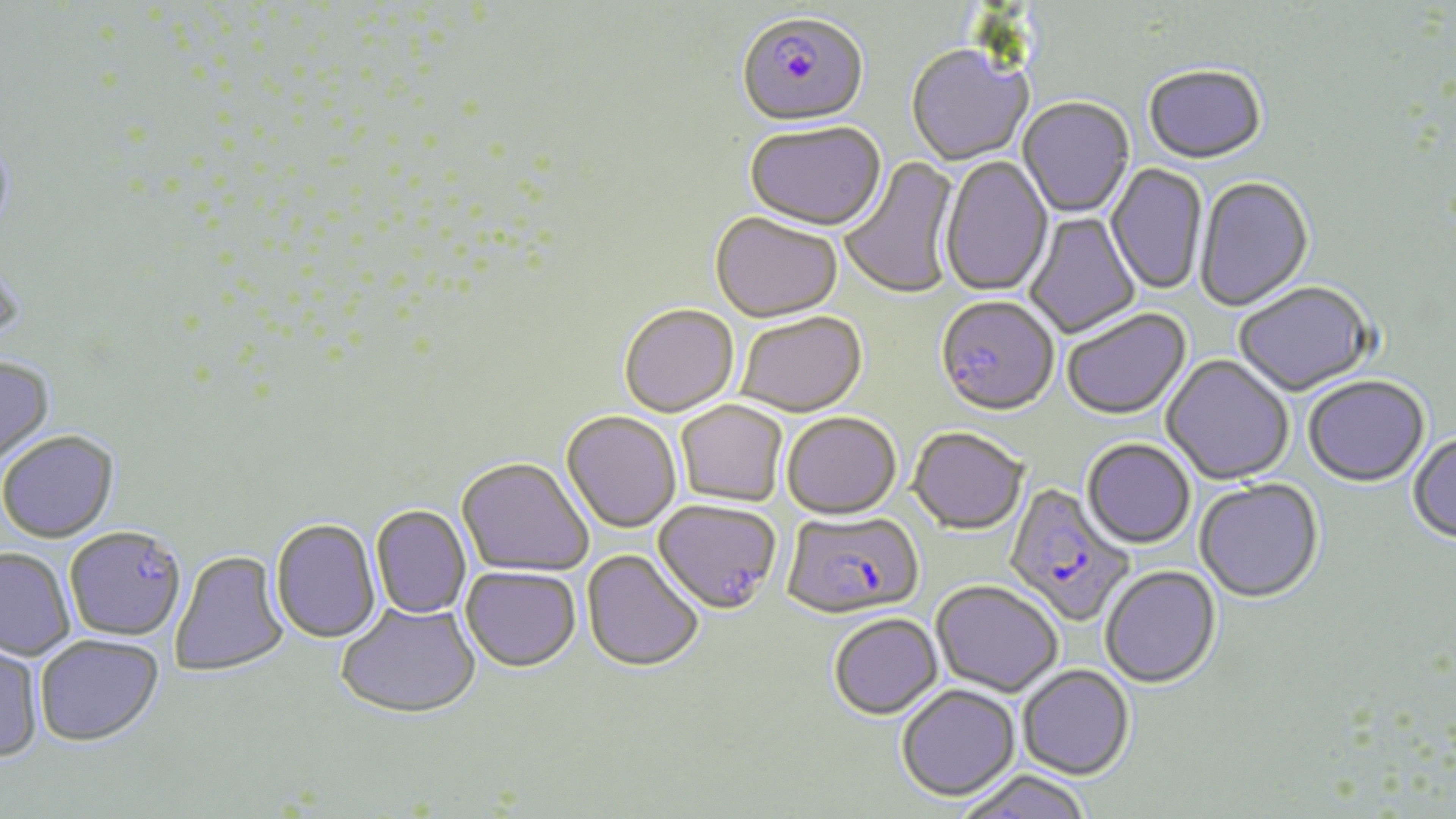

Approximate bounding boxes as named x1/y1/x2/y2 corners in pixels. Uninfected red blood cell locations: (x1=906, y1=46, x2=1033, y2=167), (x1=1143, y1=67, x2=1267, y2=167), (x1=1018, y1=98, x2=1134, y2=219), (x1=744, y1=125, x2=886, y2=234), (x1=840, y1=156, x2=962, y2=300), (x1=939, y1=156, x2=1054, y2=297), (x1=1106, y1=163, x2=1208, y2=296), (x1=1194, y1=177, x2=1315, y2=313), (x1=1024, y1=212, x2=1140, y2=339), (x1=710, y1=214, x2=844, y2=325), (x1=1233, y1=283, x2=1377, y2=398), (x1=941, y1=301, x2=1060, y2=416), (x1=619, y1=306, x2=739, y2=418), (x1=1062, y1=309, x2=1192, y2=421), (x1=737, y1=313, x2=866, y2=418), (x1=1162, y1=355, x2=1294, y2=486), (x1=0, y1=357, x2=56, y2=471), (x1=1303, y1=377, x2=1430, y2=488), (x1=676, y1=401, x2=788, y2=506), (x1=561, y1=411, x2=681, y2=533), (x1=781, y1=413, x2=902, y2=520), (x1=908, y1=426, x2=1028, y2=535), (x1=1408, y1=432, x2=1456, y2=546), (x1=0, y1=433, x2=119, y2=544), (x1=1082, y1=438, x2=1196, y2=549), (x1=456, y1=458, x2=593, y2=578), (x1=1194, y1=478, x2=1324, y2=604), (x1=653, y1=500, x2=781, y2=616), (x1=370, y1=505, x2=471, y2=619), (x1=270, y1=519, x2=382, y2=645), (x1=65, y1=527, x2=186, y2=642), (x1=0, y1=548, x2=75, y2=661), (x1=170, y1=550, x2=290, y2=678), (x1=581, y1=550, x2=704, y2=674), (x1=1100, y1=565, x2=1221, y2=689), (x1=461, y1=566, x2=581, y2=672), (x1=932, y1=579, x2=1062, y2=696), (x1=336, y1=601, x2=480, y2=719), (x1=828, y1=613, x2=943, y2=719), (x1=34, y1=634, x2=164, y2=746), (x1=0, y1=638, x2=44, y2=763), (x1=1017, y1=664, x2=1135, y2=779), (x1=896, y1=684, x2=1020, y2=801), (x1=954, y1=770, x2=1094, y2=819). Plasmodium falciparum-infected red blood cell locations: (x1=736, y1=15, x2=868, y2=132), (x1=1003, y1=482, x2=1136, y2=627), (x1=782, y1=510, x2=923, y2=620). Slide-level diagnosis: Plasmodium falciparum. One field of a larger specimen. Thin blood film. Image is 1456×819 pixels. Captured at 1000x magnification. May-Grünwald-Giemsa stain. Optical microscopy.